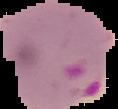
Summary:
  - Image type: cell region segmented out of the field of view; surrounding area masked to black
  - Result: Plasmodium parasites detected
  - Preparation: thin blood smear
  - Image size: 118×109 pixels